Assess this cell for malaria.
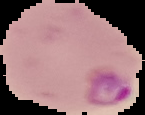

Parasitized.

preparation = thin blood smear
image type = segmented cell region on a black background
image size = 145×115 pixels